Classify this cell by malaria status.
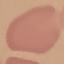

Uninfected.

Acquired by smartphone through the microscope eyepiece. Thin smear of blood. Automatically extracted cell patch, resized to 64 × 64 pixels. Giemsa stain.